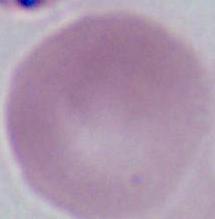

identification = red blood cell
modality = photomicrograph
magnification = 1000x